Locate every white blood cell.
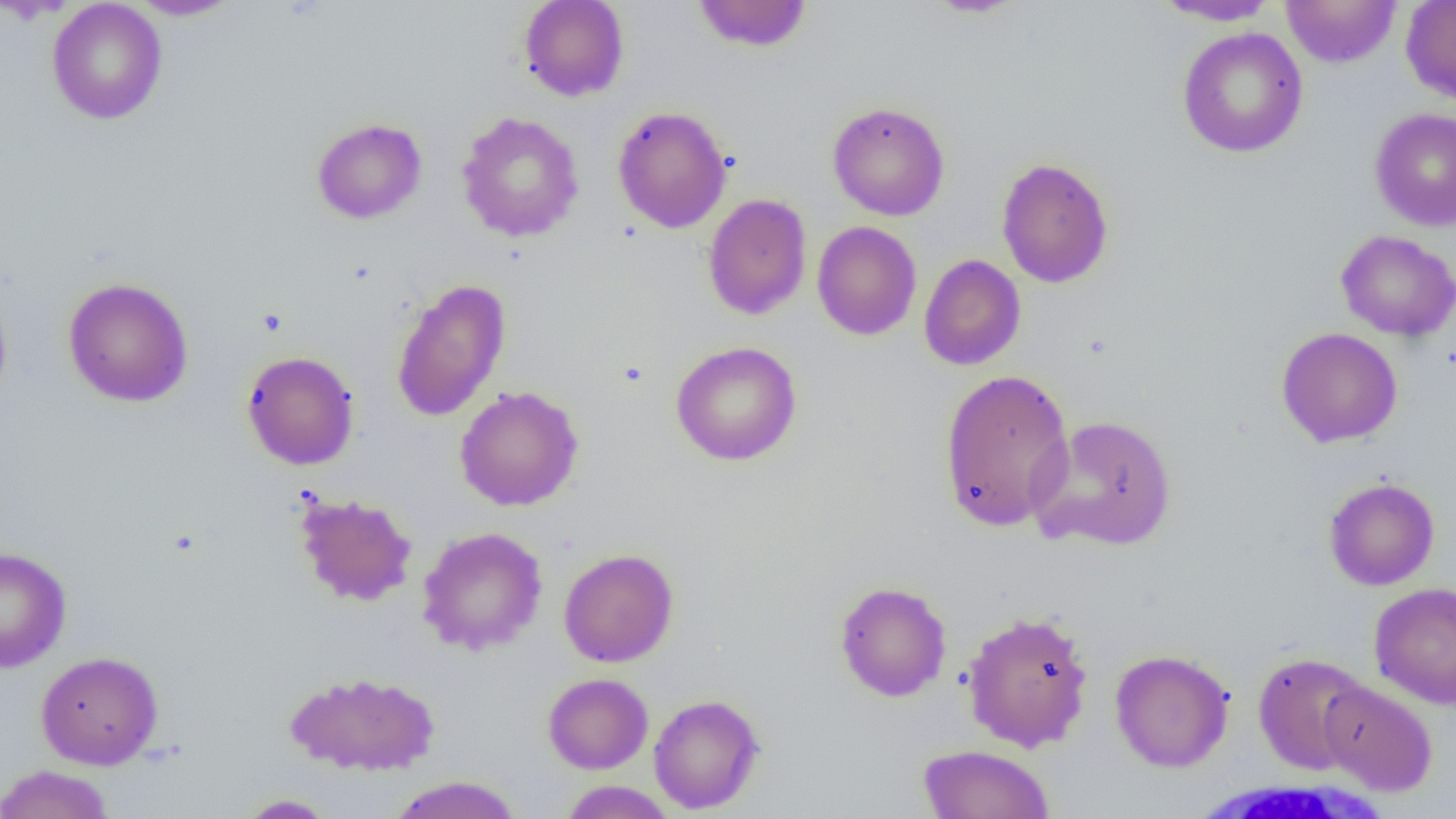
Approximate bounding boxes as [x1, y1, x2, y2] in pixels.
White blood cells: [1190, 775, 1391, 819].

slide-level diagnosis = no evidence of blood parasites
uninfected red blood cell locations = approximate bounding boxes as [x1, y1, x2, y2] in pixels: [128, 0, 243, 20], [518, 0, 630, 101], [691, 0, 813, 53], [922, 0, 1029, 18], [1281, 0, 1400, 68], [1401, 0, 1456, 104], [47, 1, 168, 125], [1153, 1, 1283, 26], [1177, 27, 1308, 158], [827, 101, 950, 221], [612, 106, 732, 234], [1370, 107, 1456, 231], [456, 111, 584, 242], [311, 118, 427, 224], [996, 157, 1114, 288], [703, 193, 812, 320], [811, 221, 922, 340], [1335, 230, 1456, 342], [918, 253, 1026, 371], [63, 277, 194, 407], [390, 278, 511, 422], [0, 286, 13, 409], [1276, 327, 1403, 447], [670, 341, 802, 466], [242, 351, 359, 470], [937, 368, 1075, 533], [454, 385, 584, 511], [1029, 414, 1178, 552], [1323, 477, 1439, 591], [294, 492, 418, 607], [417, 526, 548, 656], [0, 545, 72, 672], [558, 548, 679, 668], [834, 580, 951, 702], [1369, 582, 1456, 709], [962, 609, 1095, 752], [1110, 649, 1235, 772], [36, 650, 163, 769], [1253, 652, 1372, 774], [284, 671, 441, 775], [542, 673, 653, 774], [1319, 679, 1438, 795], [649, 694, 764, 814], [917, 744, 1054, 819], [0, 765, 116, 819], [388, 775, 524, 819], [558, 781, 677, 818], [236, 794, 336, 818]
field of view = one of a larger specimen
preparation = thin blood smear
image size = 1456×819 pixels
modality = light microscopy
magnification = 1000x